Identify the parasite.
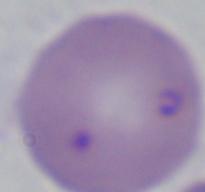

This is Babesia.

Photomicrograph. Captured at 1000x magnification.